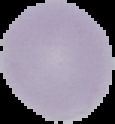

image type = cell region segmented out of the field of view; surrounding area masked to black
preparation = thin blood smear
image size = 115×124 pixels
result = no Plasmodium parasites detected